Locate every Plasmodium parasite.
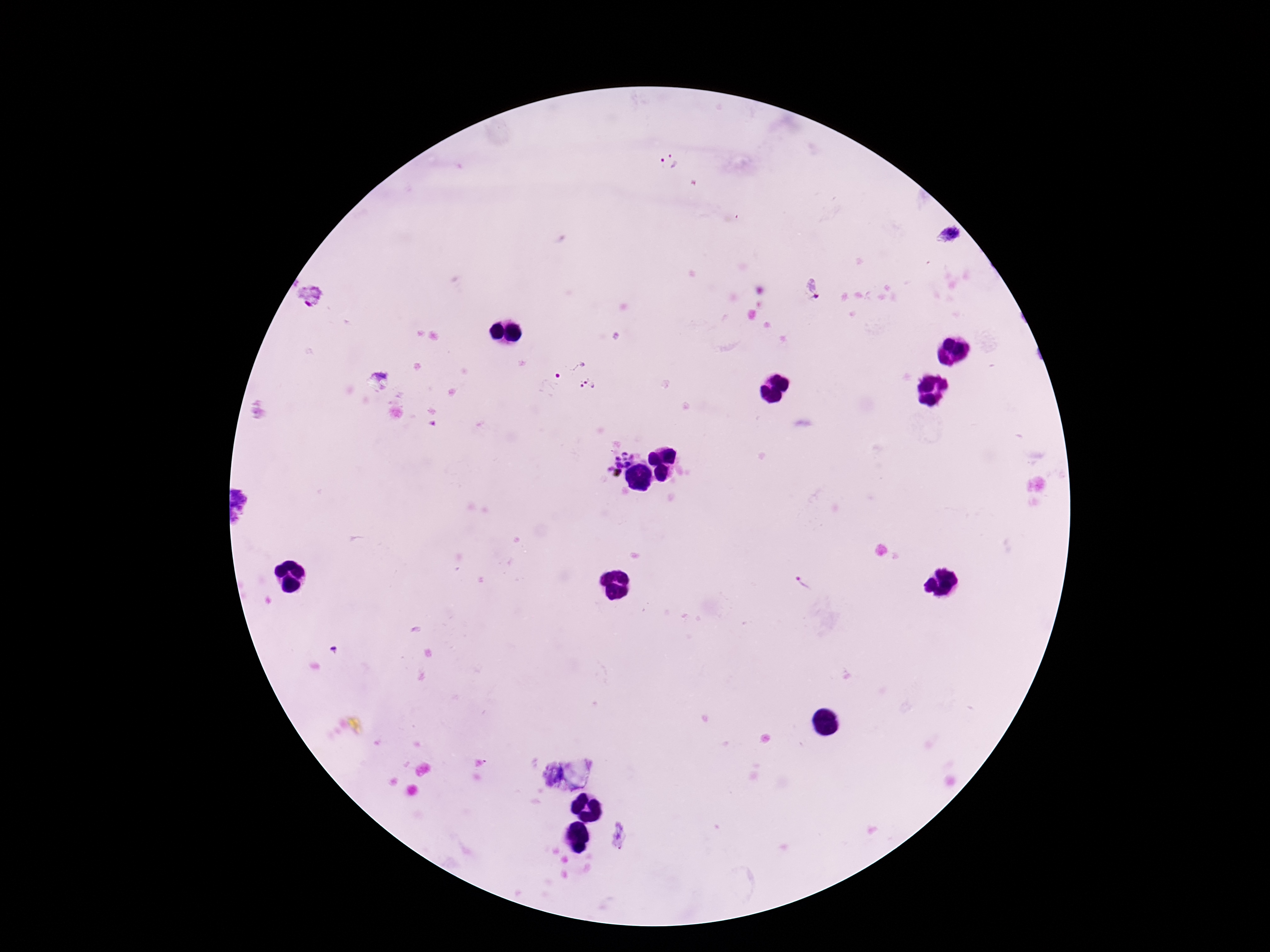

Approximate centers as {x, y} in pixels.
Plasmodium parasites: {668, 162}, {947, 235}, {813, 291}, {310, 299}, {566, 363}, {378, 383}, {589, 385}, {616, 456}, {804, 583}.

Summary:
  - Patient malaria status: positive
  - Preparation: thick peripheral-blood smear
  - Capture: smartphone camera through the microscope eyepiece
  - Image size: 1270×952 pixels
  - Field of view: one from this slide
  - Magnification: 100x
  - Stain: Giemsa